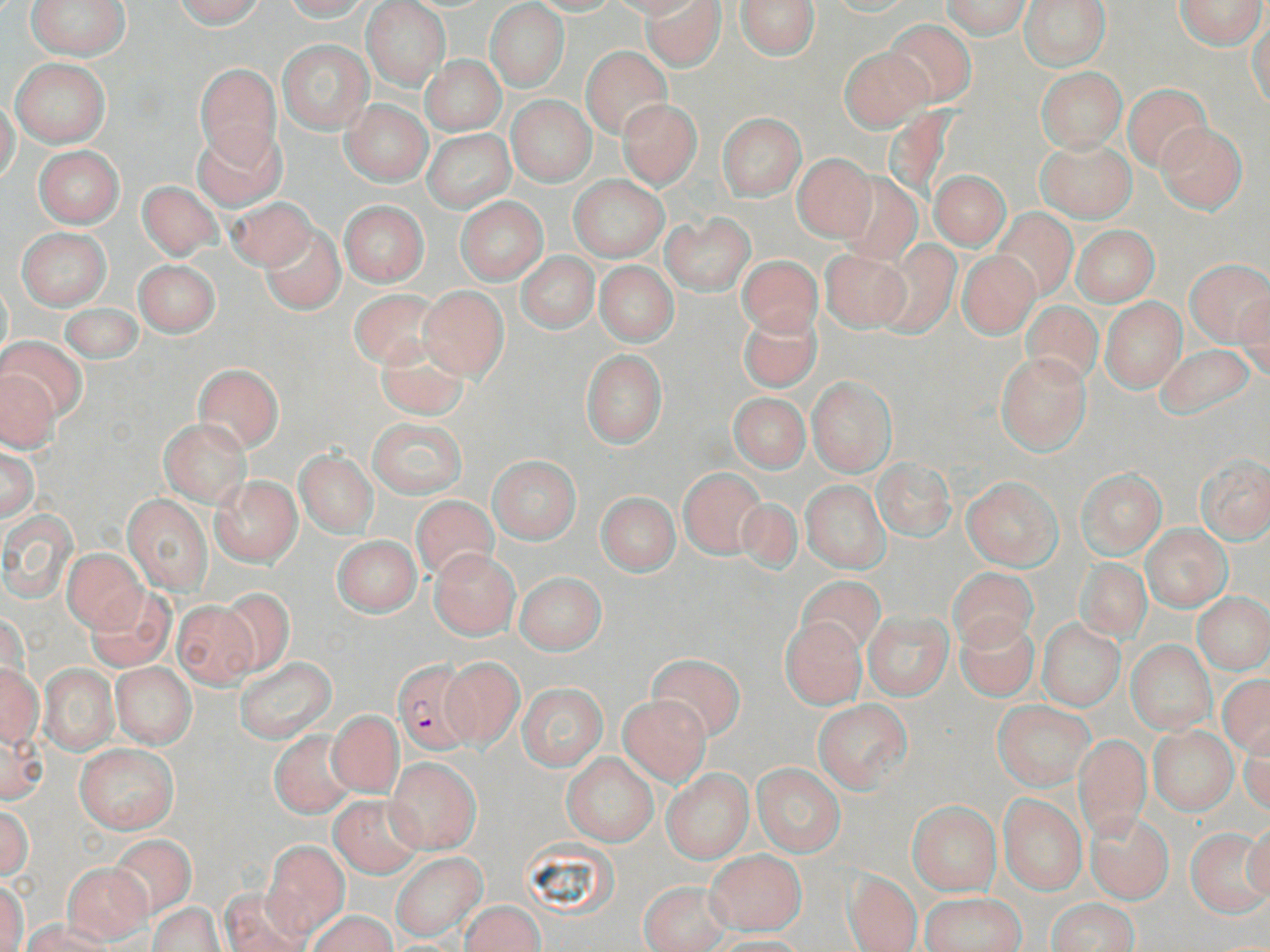

Summary:
  - Coordinate format: approximate bounding boxes as named x1/y1/x2/y2 corners in pixels
  - Plasmodium falciparum-infected red blood cell locations: (x1=392, y1=662, x2=474, y2=754)
  - Uninfected red blood cell locations: (x1=28, y1=0, x2=130, y2=60), (x1=174, y1=0, x2=265, y2=28), (x1=281, y1=0, x2=372, y2=20), (x1=528, y1=0, x2=619, y2=16), (x1=606, y1=0, x2=704, y2=18), (x1=643, y1=0, x2=725, y2=71), (x1=735, y1=0, x2=820, y2=60), (x1=942, y1=0, x2=1030, y2=39), (x1=1021, y1=0, x2=1110, y2=69), (x1=1174, y1=0, x2=1267, y2=50), (x1=361, y1=1, x2=451, y2=92), (x1=485, y1=2, x2=570, y2=92), (x1=1248, y1=15, x2=1269, y2=110), (x1=883, y1=19, x2=977, y2=106), (x1=278, y1=40, x2=372, y2=132), (x1=581, y1=47, x2=672, y2=139), (x1=838, y1=47, x2=931, y2=132), (x1=421, y1=55, x2=505, y2=136), (x1=11, y1=56, x2=110, y2=147), (x1=196, y1=64, x2=280, y2=164), (x1=1036, y1=67, x2=1126, y2=153), (x1=1123, y1=84, x2=1211, y2=170), (x1=506, y1=96, x2=596, y2=186), (x1=0, y1=100, x2=20, y2=184), (x1=341, y1=100, x2=431, y2=186), (x1=616, y1=100, x2=702, y2=189), (x1=718, y1=113, x2=807, y2=200), (x1=1156, y1=122, x2=1247, y2=213), (x1=192, y1=127, x2=285, y2=210), (x1=424, y1=130, x2=515, y2=212), (x1=1037, y1=140, x2=1135, y2=222), (x1=34, y1=145, x2=123, y2=227), (x1=793, y1=153, x2=878, y2=242), (x1=835, y1=170, x2=923, y2=264), (x1=929, y1=170, x2=1010, y2=250), (x1=570, y1=174, x2=668, y2=261), (x1=138, y1=181, x2=221, y2=260), (x1=231, y1=198, x2=318, y2=271), (x1=456, y1=198, x2=547, y2=283), (x1=339, y1=201, x2=429, y2=286), (x1=993, y1=209, x2=1076, y2=299), (x1=662, y1=213, x2=754, y2=294), (x1=1072, y1=225, x2=1158, y2=306), (x1=261, y1=226, x2=345, y2=313), (x1=17, y1=229, x2=110, y2=309), (x1=877, y1=242, x2=961, y2=336), (x1=819, y1=246, x2=909, y2=332), (x1=957, y1=250, x2=1039, y2=338), (x1=516, y1=251, x2=598, y2=332), (x1=737, y1=255, x2=822, y2=336), (x1=1185, y1=259, x2=1270, y2=344), (x1=134, y1=260, x2=220, y2=337), (x1=595, y1=262, x2=678, y2=346), (x1=420, y1=286, x2=508, y2=380), (x1=348, y1=289, x2=444, y2=369), (x1=1235, y1=295, x2=1270, y2=380), (x1=1101, y1=297, x2=1186, y2=392), (x1=1021, y1=301, x2=1102, y2=387), (x1=59, y1=303, x2=143, y2=366), (x1=737, y1=308, x2=822, y2=392), (x1=2, y1=337, x2=87, y2=420), (x1=372, y1=337, x2=473, y2=420), (x1=1154, y1=344, x2=1257, y2=420), (x1=580, y1=351, x2=666, y2=447), (x1=994, y1=351, x2=1092, y2=457), (x1=192, y1=364, x2=283, y2=452), (x1=0, y1=369, x2=58, y2=453), (x1=807, y1=376, x2=896, y2=477), (x1=727, y1=393, x2=809, y2=472), (x1=368, y1=417, x2=467, y2=498), (x1=160, y1=419, x2=250, y2=505), (x1=1, y1=445, x2=39, y2=522), (x1=296, y1=451, x2=377, y2=538), (x1=487, y1=454, x2=582, y2=543), (x1=1195, y1=455, x2=1270, y2=544), (x1=872, y1=458, x2=955, y2=539), (x1=678, y1=468, x2=767, y2=558), (x1=1077, y1=469, x2=1166, y2=557), (x1=210, y1=475, x2=302, y2=567), (x1=962, y1=477, x2=1062, y2=570), (x1=802, y1=481, x2=888, y2=572), (x1=597, y1=492, x2=679, y2=575), (x1=121, y1=493, x2=213, y2=594), (x1=410, y1=496, x2=497, y2=583), (x1=735, y1=497, x2=803, y2=575), (x1=1, y1=507, x2=79, y2=603), (x1=1142, y1=525, x2=1229, y2=610), (x1=333, y1=536, x2=421, y2=616), (x1=62, y1=549, x2=145, y2=632), (x1=429, y1=549, x2=520, y2=639), (x1=1076, y1=559, x2=1151, y2=642), (x1=949, y1=566, x2=1036, y2=650), (x1=515, y1=572, x2=606, y2=655), (x1=798, y1=577, x2=884, y2=657), (x1=87, y1=586, x2=175, y2=671), (x1=217, y1=589, x2=295, y2=676), (x1=1194, y1=594, x2=1270, y2=673), (x1=171, y1=600, x2=256, y2=687), (x1=864, y1=611, x2=952, y2=699), (x1=955, y1=616, x2=1039, y2=702), (x1=780, y1=618, x2=865, y2=709), (x1=1038, y1=621, x2=1124, y2=709), (x1=1126, y1=640, x2=1216, y2=734), (x1=647, y1=654, x2=746, y2=741), (x1=440, y1=656, x2=525, y2=749), (x1=235, y1=657, x2=337, y2=742), (x1=111, y1=662, x2=196, y2=748), (x1=0, y1=663, x2=42, y2=747), (x1=40, y1=663, x2=118, y2=755), (x1=1218, y1=675, x2=1270, y2=758), (x1=516, y1=683, x2=608, y2=770), (x1=618, y1=694, x2=711, y2=785), (x1=813, y1=700, x2=911, y2=794), (x1=992, y1=702, x2=1094, y2=790), (x1=326, y1=710, x2=403, y2=797), (x1=1239, y1=723, x2=1269, y2=816), (x1=1149, y1=726, x2=1237, y2=814), (x1=0, y1=727, x2=47, y2=805), (x1=270, y1=730, x2=358, y2=817), (x1=1075, y1=735, x2=1150, y2=841), (x1=74, y1=743, x2=178, y2=834), (x1=562, y1=752, x2=658, y2=846), (x1=387, y1=756, x2=481, y2=854), (x1=751, y1=764, x2=845, y2=856), (x1=660, y1=768, x2=753, y2=862), (x1=998, y1=793, x2=1086, y2=895), (x1=329, y1=794, x2=424, y2=877), (x1=908, y1=801, x2=1001, y2=895), (x1=0, y1=804, x2=33, y2=881), (x1=1087, y1=811, x2=1173, y2=903), (x1=1243, y1=820, x2=1270, y2=905), (x1=1186, y1=829, x2=1269, y2=917), (x1=108, y1=834, x2=196, y2=919), (x1=263, y1=840, x2=349, y2=938), (x1=390, y1=852, x2=486, y2=940), (x1=706, y1=852, x2=806, y2=934), (x1=62, y1=862, x2=151, y2=943), (x1=638, y1=869, x2=803, y2=945), (x1=844, y1=871, x2=922, y2=952), (x1=0, y1=881, x2=28, y2=952), (x1=640, y1=881, x2=730, y2=952), (x1=221, y1=885, x2=313, y2=952), (x1=922, y1=892, x2=1026, y2=952), (x1=1044, y1=899, x2=1137, y2=951), (x1=461, y1=900, x2=545, y2=951), (x1=150, y1=902, x2=226, y2=952), (x1=308, y1=911, x2=396, y2=952), (x1=20, y1=921, x2=112, y2=952), (x1=705, y1=935, x2=808, y2=952)
  - Slide-level diagnosis: Plasmodium falciparum
  - Field of view: one of a larger specimen
  - Image size: 1270×952 pixels
  - Stain: May-Grünwald-Giemsa
  - Preparation: thin blood film
  - Magnification: 1000x
  - Modality: light microscopy